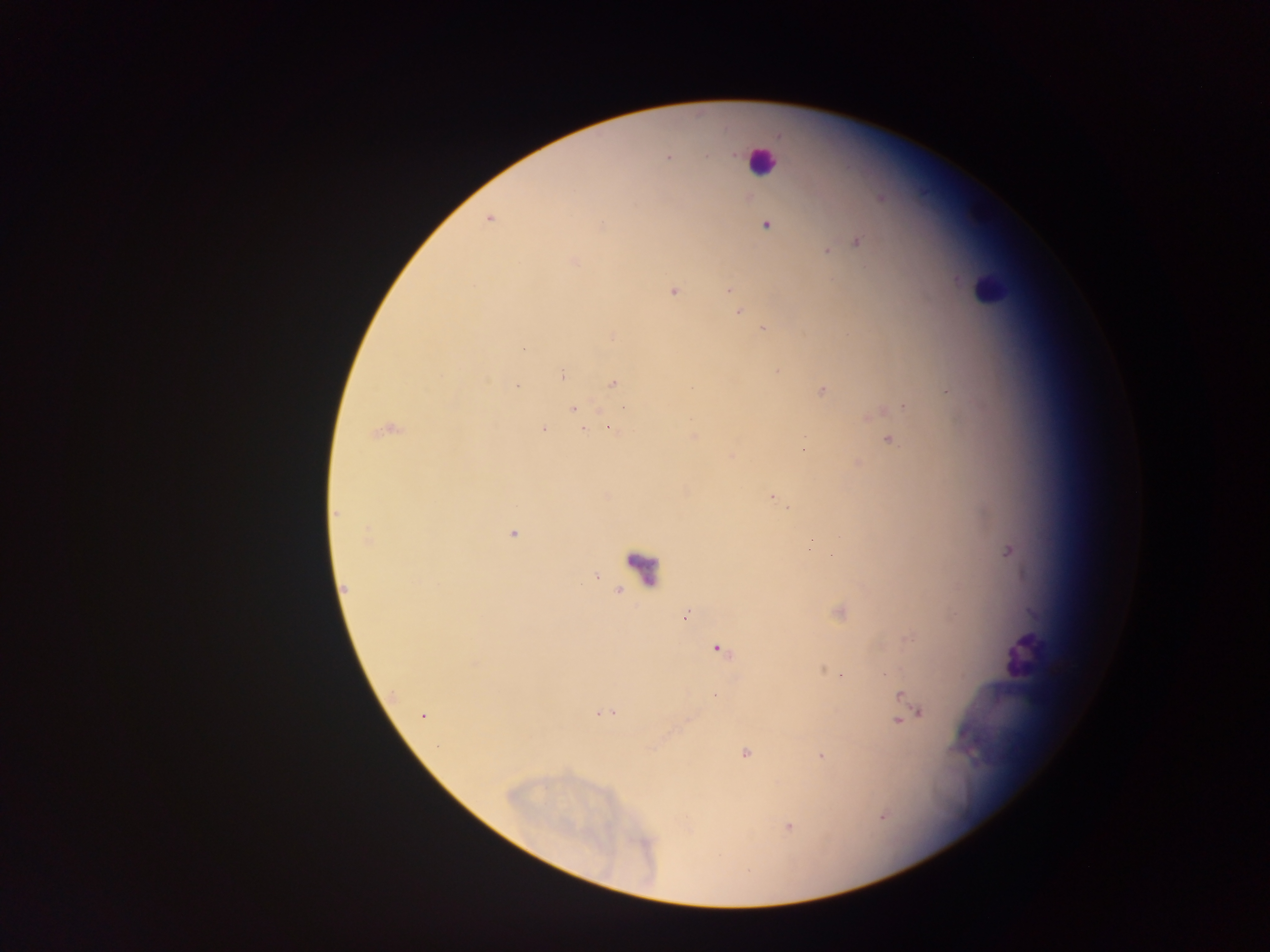

{
  "malaria_parasite_locations": "approximate centers as (x, y) in pixels: (668, 157), (489, 220), (601, 225), (766, 226), (856, 241), (827, 251), (574, 262), (729, 290), (673, 292), (739, 311), (764, 329), (614, 335), (524, 349), (563, 373), (613, 383), (517, 387), (822, 390), (948, 391), (904, 406), (625, 408), (573, 410), (575, 414), (542, 429), (611, 429), (583, 430), (381, 432), (694, 437), (889, 439), (804, 448), (772, 497), (789, 507), (336, 514), (512, 533), (367, 540), (812, 540), (1009, 551), (596, 576), (345, 589), (841, 612), (686, 615), (720, 651), (841, 675), (715, 696), (901, 696), (918, 712), (603, 714), (423, 715), (898, 721), (745, 754), (821, 756), (789, 827)",
  "leukocyte_locations": "approximate centers as (x, y) in pixels: (761, 159), (989, 290), (644, 571), (1026, 654)",
  "field_of_view": "single",
  "preparation": "thick blood film",
  "capture": "mobile-phone photograph through a microscope",
  "country": "Ghana",
  "image_size": "1270×952 pixels"
}